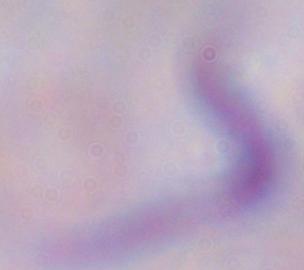
Micrograph. 1000x magnification. A trypanosome is shown.